Classify this cell by malaria status.
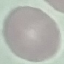
It is uninfected.

Giemsa stain. Automatically extracted cell patch, resized to 64 × 64 pixels. Thin blood smear. Acquired by smartphone through the microscope eyepiece.